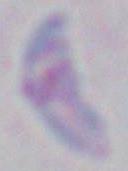

1000x magnification. Toxoplasma gondii is shown. Photomicrograph.